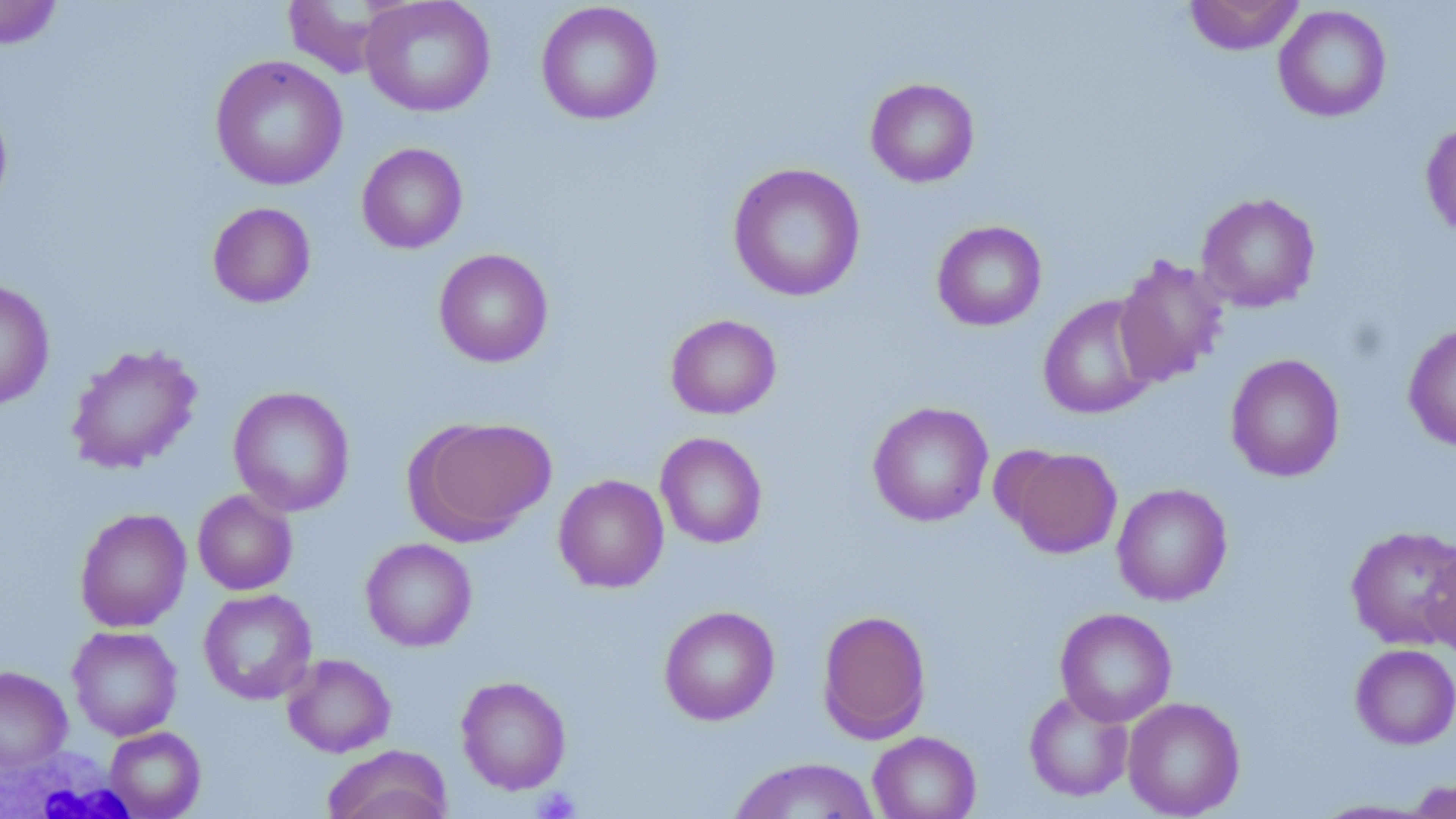
Approximate bounding boxes as named x1/y1/x2/y2 corners in pixels. White blood cell locations: (x1=0, y1=745, x2=143, y2=819). Uninfected red blood cell locations: (x1=360, y1=0, x2=496, y2=117), (x1=1184, y1=0, x2=1305, y2=55), (x1=0, y1=1, x2=64, y2=50), (x1=281, y1=1, x2=395, y2=78), (x1=535, y1=2, x2=663, y2=125), (x1=1273, y1=5, x2=1392, y2=122), (x1=210, y1=55, x2=348, y2=191), (x1=865, y1=78, x2=980, y2=187), (x1=0, y1=97, x2=13, y2=215), (x1=1420, y1=118, x2=1456, y2=240), (x1=356, y1=143, x2=468, y2=254), (x1=727, y1=162, x2=866, y2=302), (x1=1196, y1=192, x2=1320, y2=313), (x1=207, y1=202, x2=316, y2=308), (x1=932, y1=220, x2=1047, y2=331), (x1=433, y1=248, x2=554, y2=367), (x1=1113, y1=254, x2=1230, y2=387), (x1=0, y1=281, x2=55, y2=410), (x1=1038, y1=295, x2=1160, y2=419), (x1=665, y1=314, x2=782, y2=419), (x1=1403, y1=322, x2=1456, y2=451), (x1=65, y1=343, x2=203, y2=474), (x1=1225, y1=353, x2=1345, y2=482), (x1=228, y1=386, x2=355, y2=516), (x1=867, y1=401, x2=993, y2=527), (x1=406, y1=416, x2=556, y2=542), (x1=655, y1=432, x2=767, y2=549), (x1=1007, y1=447, x2=1122, y2=558), (x1=553, y1=473, x2=669, y2=593), (x1=1111, y1=483, x2=1233, y2=606), (x1=192, y1=489, x2=298, y2=595), (x1=74, y1=507, x2=192, y2=632), (x1=1346, y1=524, x2=1456, y2=650), (x1=360, y1=538, x2=477, y2=652), (x1=1423, y1=544, x2=1456, y2=662), (x1=198, y1=588, x2=317, y2=705), (x1=658, y1=605, x2=780, y2=725), (x1=1054, y1=607, x2=1177, y2=727), (x1=817, y1=609, x2=931, y2=743), (x1=67, y1=625, x2=182, y2=741), (x1=1351, y1=643, x2=1456, y2=749), (x1=282, y1=653, x2=396, y2=757), (x1=0, y1=666, x2=72, y2=771), (x1=456, y1=675, x2=572, y2=795), (x1=1024, y1=688, x2=1134, y2=802), (x1=1123, y1=696, x2=1245, y2=818), (x1=104, y1=726, x2=206, y2=818), (x1=867, y1=731, x2=981, y2=819), (x1=322, y1=744, x2=453, y2=819), (x1=728, y1=757, x2=881, y2=818), (x1=1401, y1=779, x2=1456, y2=817). Platelet locations: (x1=534, y1=786, x2=580, y2=819). Slide-level diagnosis: no evidence of blood parasites. Thin blood film. May-Grünwald-Giemsa stain. Image is 1456×819 pixels. Optical microscopy. Single field of view. 1000x magnification.